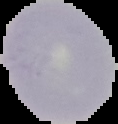
Summary:
  - Preparation: thin blood film
  - Malaria status: uninfected
  - Image size: 118×124 pixels
  - Image type: cell region segmented out of the field of view; surrounding area masked to black